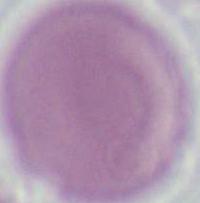

identification = erythrocyte
modality = micrograph
magnification = 1000x